Classify this cell by malaria status.
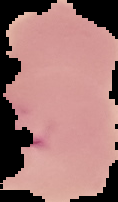
Parasitized.

{
  "image_size": "118×202 pixels",
  "image_type": "segmented cell region on a black background",
  "preparation": "thin blood smear"
}